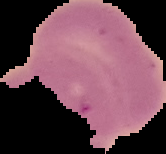

image type = cell region segmented out of the field of view; surrounding area masked to black
preparation = thin blood smear
malaria status = uninfected
image size = 166×154 pixels